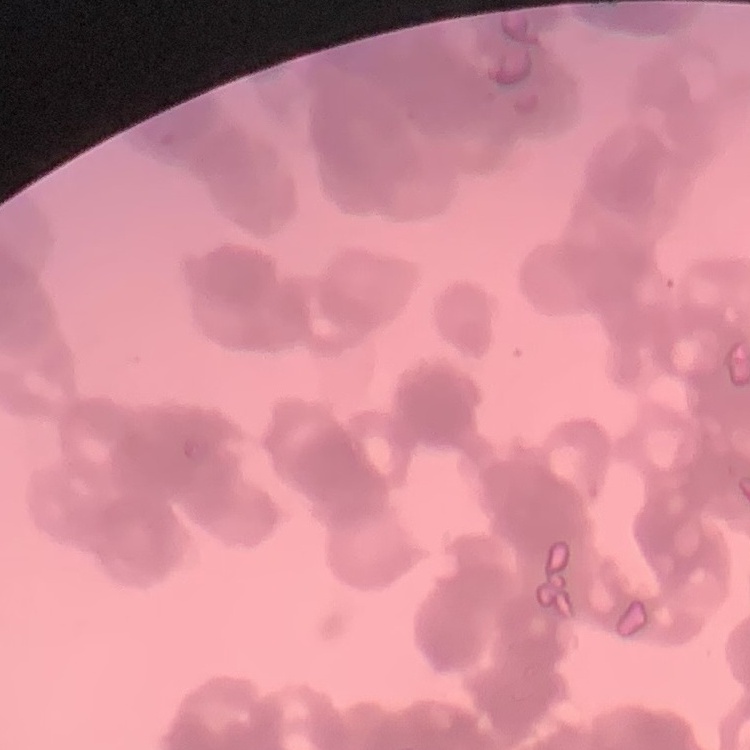
Summary:
  - Red blood cell morphology: rouleaux formation
  - Preparation: thin blood film
  - Stain: Field's or Giemsa
  - Image type: one tile cut from a larger photomicrograph